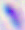
400x magnification. Micrograph. Toxoplasma gondii is seen.